Locate the cells, classifying each as a parasitized red blood cell, an uninfected red blood cell, or a white blood cell.
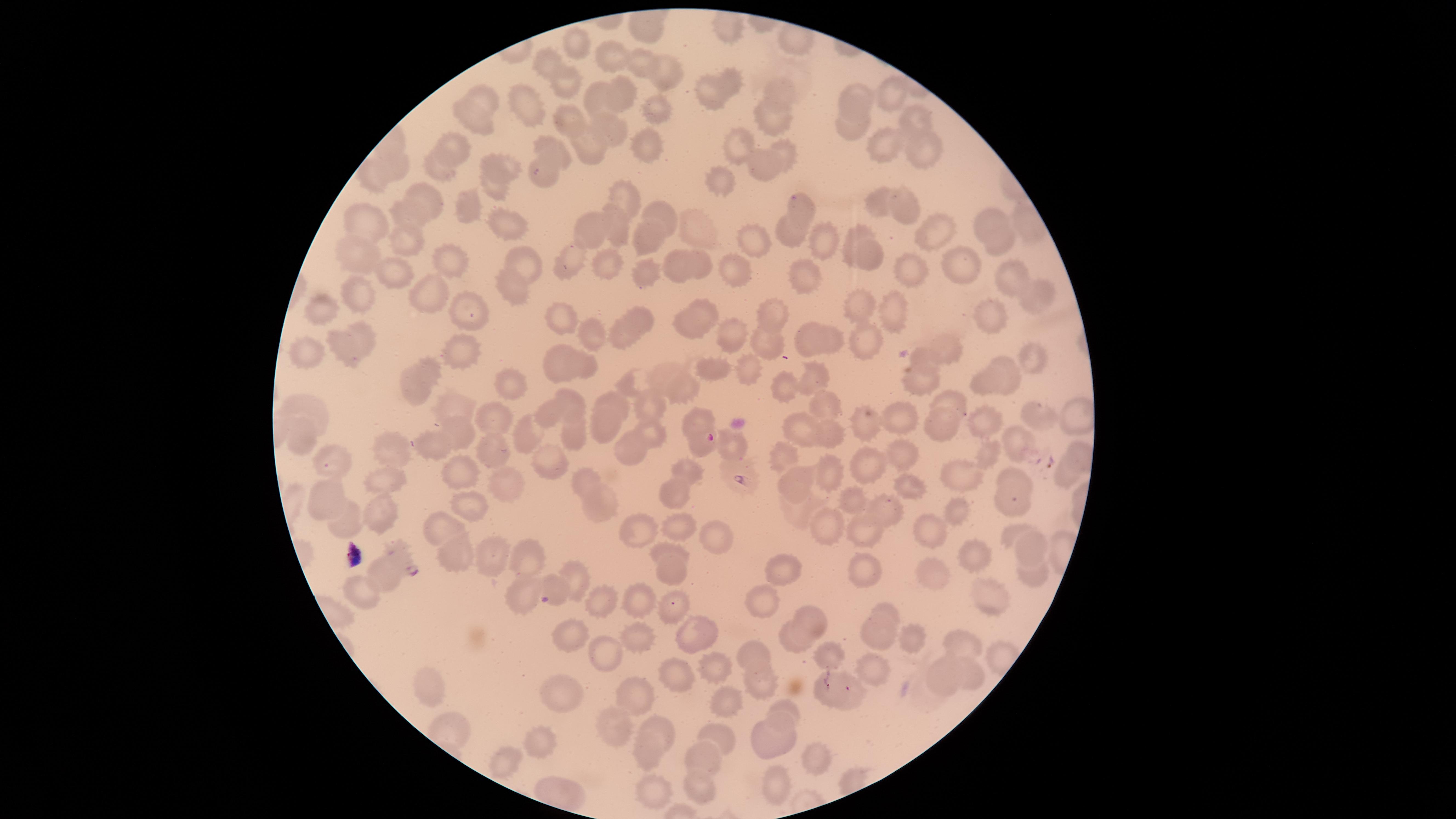

Approximate marker points as [x, y] in pixels.
Parasitized red blood cells: [708, 437], [326, 465], [407, 563].
Uninfected red blood cells: [573, 44], [607, 57], [543, 63], [638, 65], [665, 72], [563, 83], [731, 83], [783, 90], [889, 91], [709, 93], [599, 96], [621, 96], [859, 98], [530, 99], [491, 103], [653, 106], [775, 117], [917, 117], [572, 119], [472, 120], [854, 124], [607, 127], [892, 146], [559, 147], [592, 147], [646, 148], [736, 148], [922, 148], [455, 150], [788, 154], [440, 167], [508, 167], [396, 168], [766, 168], [373, 177], [547, 179], [490, 183], [721, 183], [622, 197], [882, 200], [427, 202], [467, 207], [910, 207], [658, 210], [803, 210], [409, 217], [989, 217], [616, 220], [503, 224], [366, 225], [594, 226], [698, 229], [936, 231], [792, 234], [854, 238], [407, 239], [647, 239], [994, 239], [751, 241], [823, 242], [361, 256], [873, 257], [519, 259], [575, 260], [450, 261], [698, 262], [674, 264], [740, 265], [607, 266], [963, 268], [397, 270], [810, 272], [647, 273], [913, 276], [1011, 276], [512, 283], [431, 295], [1036, 296], [358, 299], [862, 307], [894, 310], [558, 311], [704, 311], [333, 312], [474, 316], [770, 316], [639, 317], [994, 317], [691, 324], [590, 332], [365, 336], [626, 336], [738, 336], [812, 338], [867, 340], [767, 341], [342, 343], [836, 344], [944, 350], [304, 355], [467, 355], [1035, 355], [556, 363], [584, 364], [718, 368], [433, 370], [746, 371], [1013, 375], [813, 376], [662, 377], [919, 380], [992, 380], [510, 381], [637, 383], [415, 387], [685, 390], [782, 391], [618, 401], [948, 402], [652, 404], [572, 406], [315, 408], [450, 410], [829, 410], [550, 411], [498, 416], [898, 417], [1039, 417], [699, 419], [985, 421], [606, 422], [944, 422], [805, 425], [867, 427], [464, 430], [532, 430], [578, 431], [653, 431], [832, 433], [299, 435], [431, 440], [1019, 444], [389, 445], [734, 445], [632, 447], [491, 450], [899, 453], [990, 453], [784, 456], [869, 461], [551, 463], [831, 470], [694, 472], [456, 473], [382, 474], [1063, 475], [1015, 476], [793, 477], [962, 479], [589, 481], [506, 484], [903, 486], [676, 492], [325, 498], [1015, 499], [380, 500], [857, 503], [600, 504], [467, 505], [799, 508], [889, 510], [956, 510], [341, 516], [820, 525], [685, 527], [446, 528], [634, 529], [862, 529], [1010, 532], [712, 535], [932, 535], [1033, 543], [662, 548], [456, 551], [528, 553], [493, 554], [973, 557], [866, 563], [791, 571], [938, 572], [1032, 574], [672, 575], [382, 578], [578, 580], [552, 587], [368, 590], [989, 591], [602, 599], [526, 600], [765, 600], [639, 602], [667, 609], [885, 614], [811, 621], [881, 630], [696, 632], [571, 636], [914, 637], [803, 639], [967, 639], [636, 641], [756, 647], [602, 655], [826, 656], [710, 661], [966, 671], [874, 672], [946, 675], [674, 678], [761, 679], [827, 687], [426, 688], [727, 696], [850, 698], [563, 699], [636, 702], [787, 712], [616, 725], [664, 728], [717, 737], [540, 741], [771, 741], [651, 752], [814, 758], [504, 762], [713, 765], [776, 784], [702, 785], [658, 788].
No white blood cells identified.

Smartphone photograph through the microscope eyepiece. Image is 1456×819 pixels. Circular visible region. Giemsa stain. Thin smear of blood. Species: Plasmodium falciparum. Single field of view.